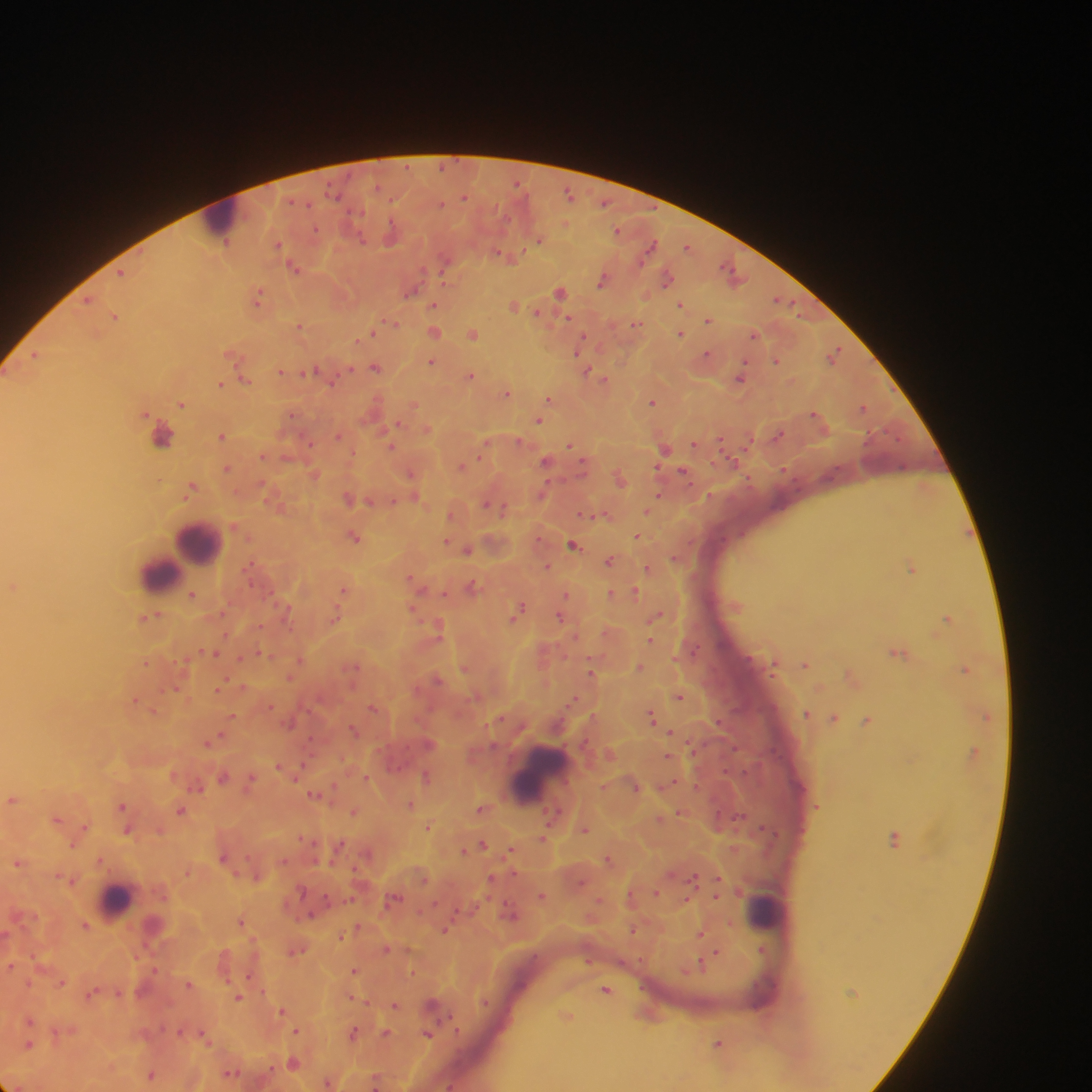
country = Ghana
leukocyte locations = approximate centers as [x, y] in pixels: [223, 217], [162, 434], [200, 542], [173, 560], [158, 573], [542, 776], [115, 899], [766, 911]
Plasmodium parasite locations = approximate centers as [x, y] in pixels: [569, 194], [464, 196], [619, 229], [392, 234], [539, 239], [279, 245], [651, 246], [688, 246], [503, 255], [446, 261], [295, 266], [120, 272], [733, 273], [667, 277], [603, 280], [411, 291], [561, 291], [259, 295], [87, 300], [782, 300], [434, 304], [515, 304], [681, 304], [539, 312], [115, 316], [708, 319], [390, 323], [636, 324], [299, 327], [434, 331], [372, 332], [473, 333], [681, 333], [755, 334], [582, 341], [835, 353], [707, 354], [36, 355], [233, 355], [433, 361], [777, 361], [376, 367], [586, 370], [282, 371], [310, 372], [471, 375], [597, 375], [741, 377], [605, 379], [245, 380], [331, 380], [221, 383], [507, 392], [550, 398], [182, 402], [654, 402], [414, 404], [863, 406], [816, 414], [539, 420], [396, 424], [428, 428], [223, 435], [338, 435], [778, 435], [721, 440], [747, 443], [695, 444], [393, 445], [570, 446], [483, 449], [665, 449], [263, 455], [547, 461], [584, 462], [461, 466], [228, 468], [314, 473], [412, 473], [684, 473], [621, 477], [924, 487], [190, 488], [543, 492], [659, 494], [415, 497], [350, 498], [370, 501], [278, 504], [487, 504], [499, 507], [647, 511], [452, 513], [586, 515], [603, 515], [235, 525], [637, 536], [354, 537], [447, 541], [574, 544], [467, 549], [676, 557], [611, 560], [251, 565], [547, 566], [912, 567], [648, 568], [416, 581], [13, 586], [473, 586], [344, 589], [445, 592], [635, 592], [611, 593], [193, 594], [566, 595], [413, 608], [287, 609], [518, 610], [151, 615], [656, 615], [336, 616], [560, 616], [948, 618], [439, 628], [651, 640], [213, 652], [899, 652], [262, 654], [300, 659], [147, 662], [775, 663], [806, 664], [353, 665], [465, 667], [640, 667], [965, 669], [592, 671], [852, 676], [290, 677], [438, 680], [224, 684], [243, 687], [175, 689], [219, 689], [679, 696], [575, 699], [135, 700], [270, 705], [375, 708], [154, 710], [807, 713], [986, 715], [233, 716], [653, 717], [500, 718], [834, 718], [868, 720], [354, 730], [671, 732], [217, 737], [212, 742], [974, 750], [610, 754], [668, 756], [280, 766], [300, 770], [427, 775], [223, 776], [366, 777], [251, 780], [198, 785], [636, 785], [667, 785], [334, 787], [316, 794], [13, 799], [411, 804], [122, 807], [482, 807], [181, 810], [354, 812], [681, 813], [661, 818], [57, 819], [429, 827], [83, 828], [127, 829], [585, 829], [159, 830], [542, 838], [896, 838], [483, 844], [339, 846], [464, 850], [512, 850], [367, 854], [224, 856], [608, 858], [101, 859], [18, 862], [186, 871], [257, 876], [717, 878], [69, 879], [491, 879], [694, 879], [655, 891], [542, 896], [631, 896], [716, 896], [394, 897], [686, 899], [511, 913], [311, 915], [241, 921], [154, 923], [85, 924], [358, 926], [446, 929], [634, 929], [700, 933], [340, 936], [386, 948], [296, 949], [762, 949], [716, 952], [588, 959], [702, 964], [10, 965], [354, 970], [413, 971], [250, 976], [62, 982], [29, 983], [189, 984], [606, 989], [93, 992], [119, 992], [239, 997], [352, 998], [486, 1001], [395, 1004], [433, 1005], [282, 1010], [567, 1016], [31, 1020], [297, 1030], [56, 1032], [181, 1032], [353, 1033], [386, 1033], [428, 1034], [205, 1035], [720, 1043], [29, 1044], [294, 1062], [231, 1072], [151, 1074], [375, 1080], [328, 1082], [450, 1085]
image size = 1092×1092 pixels
preparation = thick blood smear
capture = mobile-phone photograph through a microscope
field of view = single